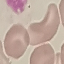 Malaria status: uninfected. Giemsa stain. Acquired by smartphone through the microscope eyepiece. Thin blood smear. Automatically extracted cell patch, resized to 64 × 64 pixels.